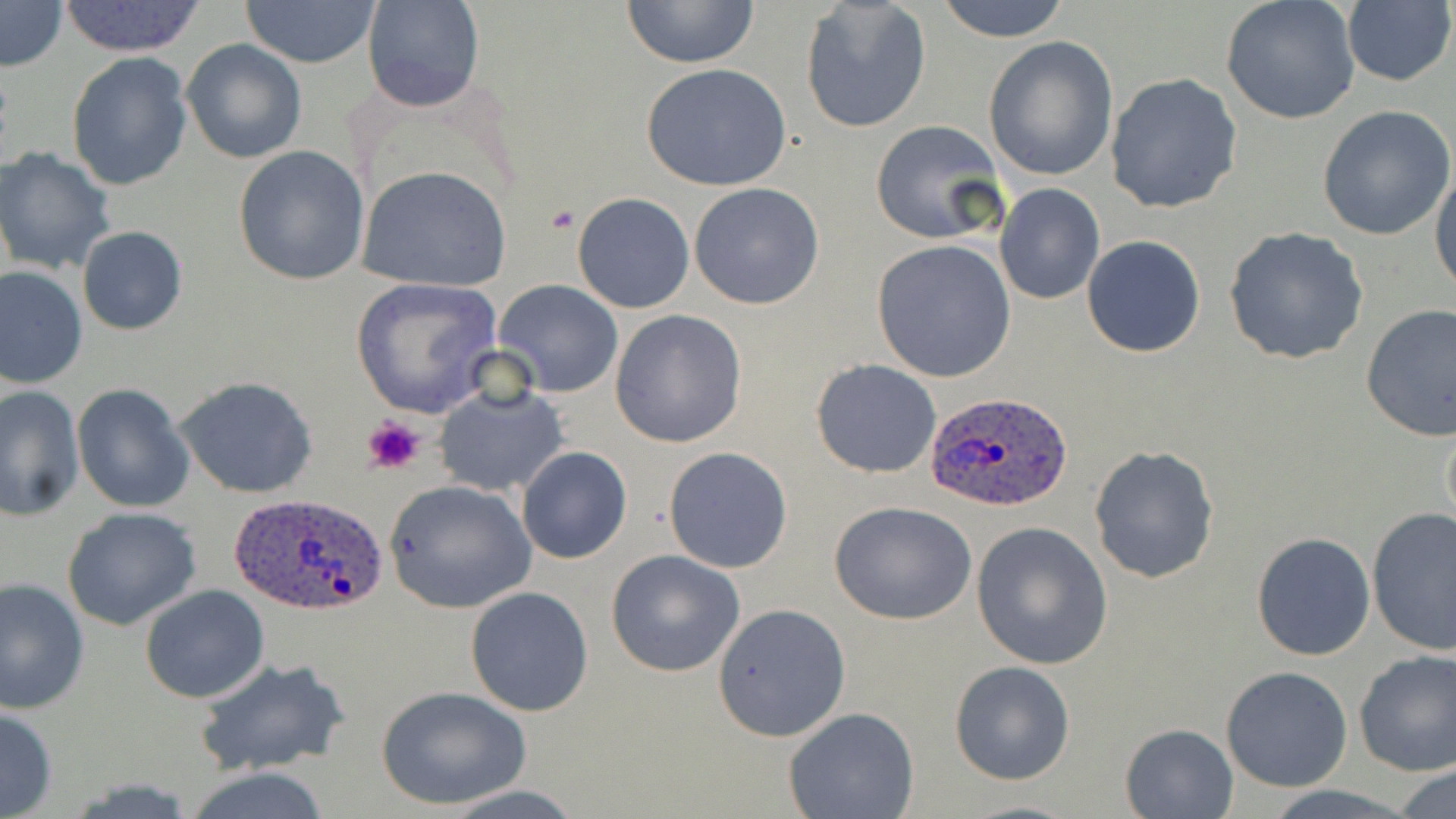

slide-level diagnosis = Plasmodium ovale
modality = optical microscopy
magnification = 1000x
uninfected red blood cell locations = approximate bounding boxes as (x1, y1, x2, y2) in pixels: (57, 0, 208, 56), (619, 0, 762, 69), (935, 0, 1073, 43), (1221, 0, 1361, 125), (1, 1, 68, 72), (241, 1, 383, 68), (363, 1, 484, 112), (799, 1, 931, 134), (1341, 3, 1455, 86), (982, 36, 1118, 181), (181, 39, 308, 166), (66, 52, 193, 192), (641, 63, 793, 192), (1105, 72, 1243, 214), (1317, 104, 1454, 241), (870, 120, 1006, 246), (232, 144, 370, 285), (0, 146, 118, 275), (1430, 160, 1455, 299), (356, 164, 513, 292), (994, 182, 1106, 304), (687, 183, 824, 311), (573, 192, 694, 314), (77, 226, 186, 336), (1223, 226, 1370, 365), (1081, 236, 1205, 356), (872, 238, 1017, 382), (0, 265, 87, 390), (349, 278, 501, 418), (493, 279, 623, 398), (1359, 302, 1456, 441), (610, 311, 747, 449), (810, 359, 943, 478), (174, 377, 319, 499), (434, 382, 569, 497), (0, 383, 84, 520), (72, 383, 193, 512), (1441, 407, 1456, 542), (1088, 445, 1219, 583), (662, 446, 792, 574), (517, 447, 633, 564), (384, 479, 538, 615), (830, 500, 978, 625), (62, 506, 202, 631), (1365, 507, 1456, 656), (971, 520, 1113, 671), (1250, 531, 1377, 661), (605, 549, 747, 678), (0, 577, 89, 718), (139, 584, 270, 703), (466, 586, 595, 717), (713, 602, 852, 741), (1354, 650, 1456, 776), (192, 657, 349, 777), (949, 661, 1076, 784), (1222, 665, 1352, 793), (374, 686, 533, 810), (0, 702, 58, 818), (783, 708, 918, 819), (1120, 723, 1237, 817), (1391, 766, 1456, 817), (439, 786, 588, 818), (957, 799, 1087, 817)
Plasmodium ovale-infected red blood cell locations = approximate bounding boxes as (x1, y1, x2, y2) in pixels: (925, 392, 1075, 513), (228, 492, 391, 617)
field of view = single
stain = May-Grünwald-Giemsa
platelet locations = approximate bounding boxes as (x1, y1, x2, y2) in pixels: (361, 413, 428, 476)
image size = 1456×819 pixels
preparation = thin blood film